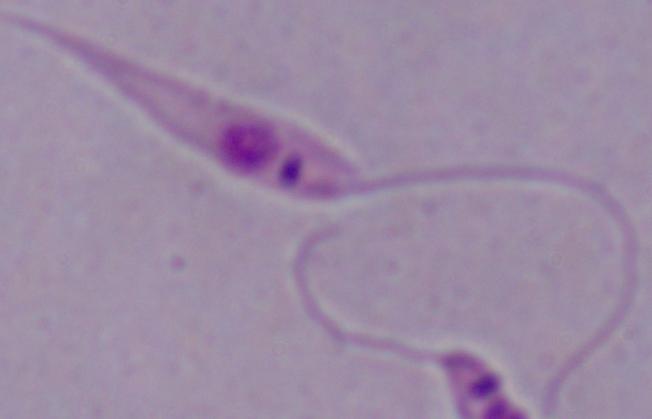
Summary:
  - Identification: Leishmania
  - Modality: micrograph
  - Magnification: 1000x